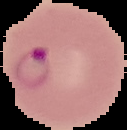
Summary:
  - Preparation: thin blood film
  - Result: malaria parasites identified
  - Image size: 127×130 pixels
  - Image type: cell region segmented out of the field of view; surrounding area masked to black